Assess this cell for malaria.
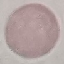

Uninfected.

Summary:
  - Stain: Giemsa
  - Preparation: thin blood smear
  - Capture: smartphone camera at the microscope eyepiece
  - Image type: cell patch, automatically extracted from a larger field of view and resized to 64 × 64 pixels